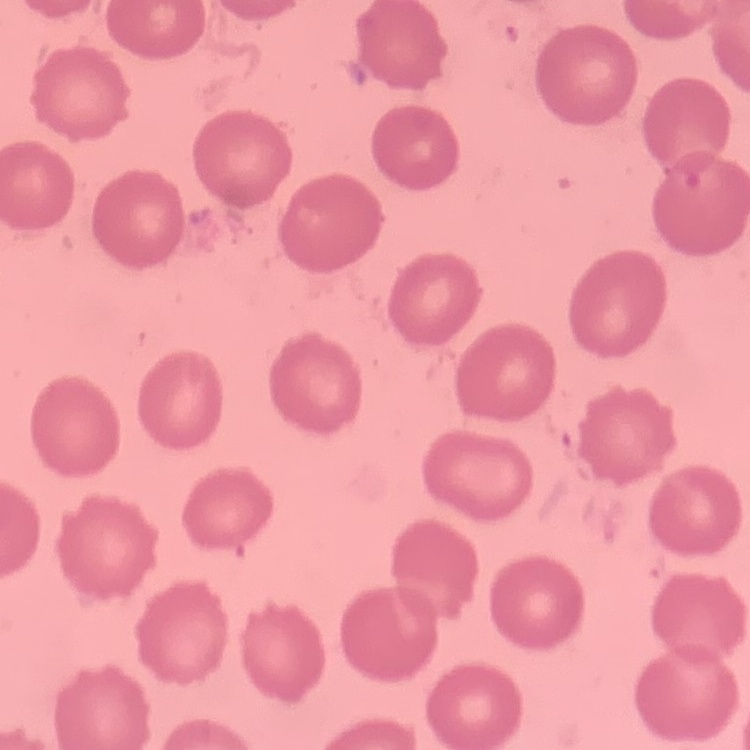
red blood cell morphology = no rouleaux formation
stain = Field's or Giemsa
image type = one tile cut from a larger photomicrograph
preparation = thin blood film